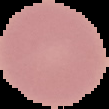

Summary:
  - Result: negative for malaria parasites
  - Image size: 109×109 pixels
  - Preparation: thin blood film
  - Image type: segmented cell region with the area outside set to black